Assess this cell for malaria.
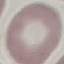
Uninfected.

Summary:
  - Preparation: thin blood smear
  - Stain: Giemsa
  - Capture: smartphone camera at the microscope eyepiece
  - Image type: cell patch, automatically extracted from a larger field of view and resized to 64 × 64 pixels